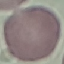

Result: no malaria parasites seen. Thin blood film. Automatically extracted cell patch, resized to 64 × 64 pixels. Photographed with a smartphone camera at the microscope eyepiece. Giemsa stain.